Assess this cell for malaria.
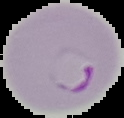
It is parasitized.

Image is 124×118 pixels. From a thin blood film. Segmented cell region on a black background.